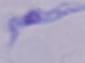

Summary:
  - Identification: trypanosome
  - Modality: photomicrograph
  - Magnification: 1000x